Report the malaria status of this cell.
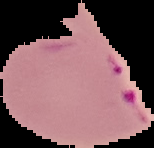
Parasitized.

Summary:
  - Image type: segmented cell region on a black background
  - Image size: 154×148 pixels
  - Preparation: thin blood film